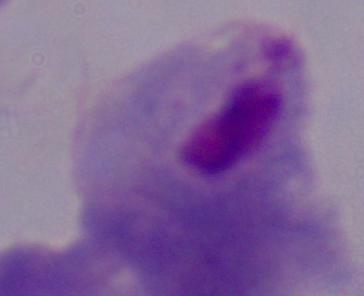
{
  "magnification": "1000x",
  "modality": "micrograph",
  "identification": "trichomonad"
}